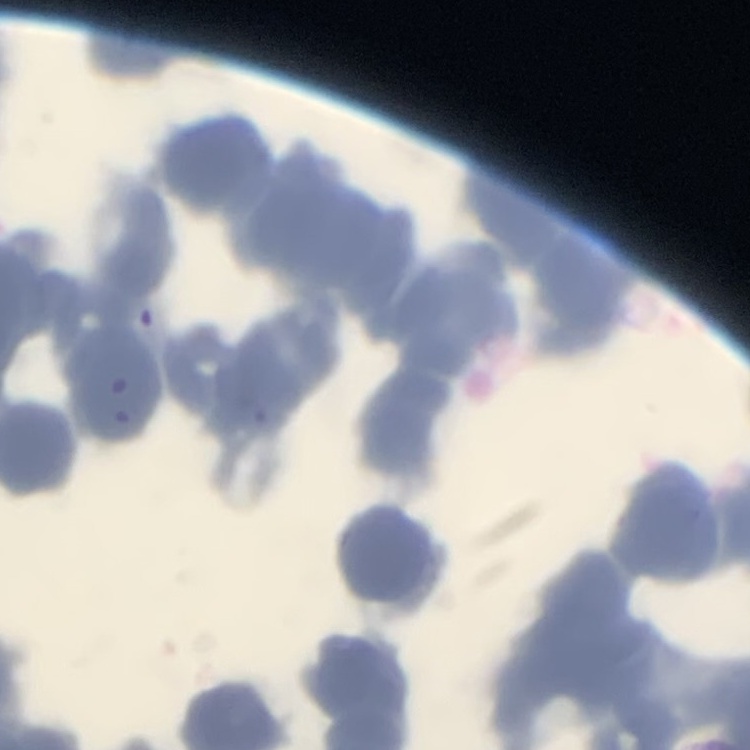

The red blood cells exhibit rouleaux formation. Stained with either Field's or Giemsa. Square crop of a larger photomicrograph. Thin blood smear.